Assess the morphology of the erythrocytes.
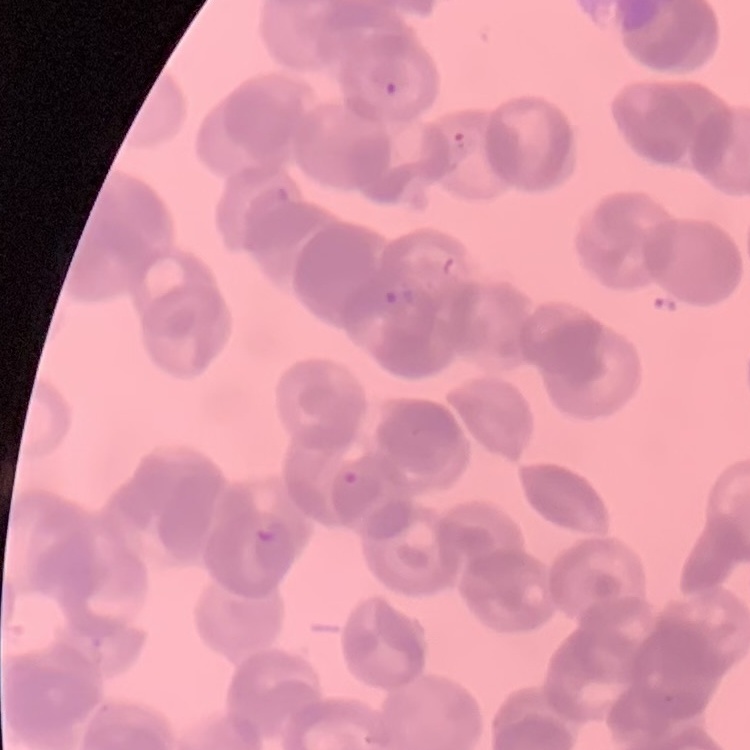
Rouleaux formation.

Summary:
  - Image type: square crop of a larger photomicrograph
  - Preparation: thin blood smear
  - Stain: Field's or Giemsa